Report the malaria status of this cell.
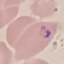

It is parasitized.

preparation: thin blood smear
capture: smartphone through the microscope eyepiece
image_type: automatically extracted cell patch, resized to 64 × 64 pixels
stain: Giemsa